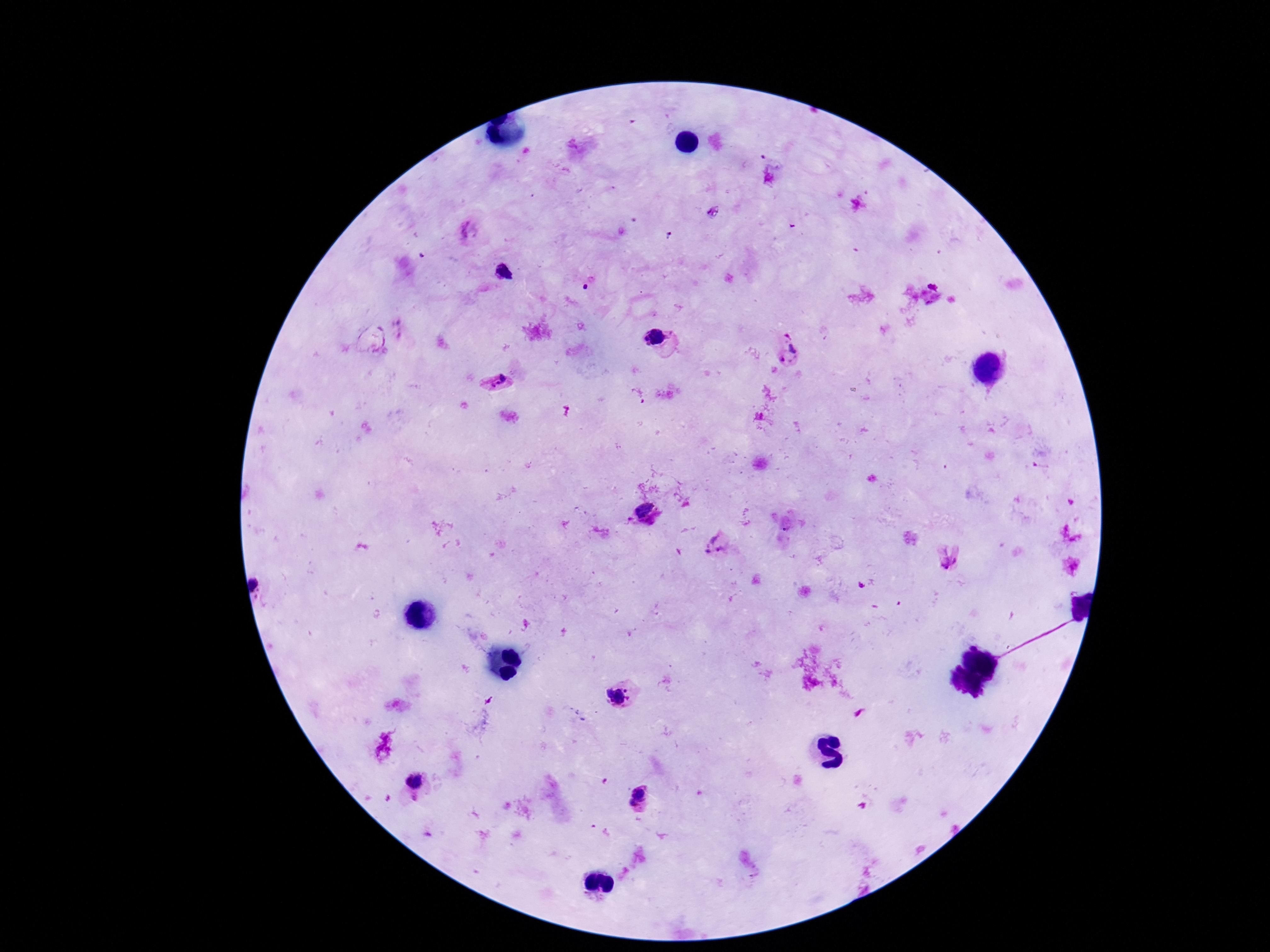
stain = Giemsa
Plasmodium parasite locations = approximate object centers, in pixels from the top-left corner: (x=467, y=231), (x=505, y=271), (x=786, y=335), (x=654, y=336), (x=794, y=347), (x=783, y=360), (x=503, y=376), (x=496, y=384), (x=642, y=508), (x=714, y=545), (x=949, y=559), (x=617, y=697), (x=414, y=781), (x=640, y=791), (x=632, y=803)
field of view = one from this slide
image size = 1270×952 pixels
magnification = 100x
patient malaria status = infected
preparation = thick peripheral-blood smear
capture = smartphone camera through the microscope eyepiece